Locate leukocytes (white blood cells).
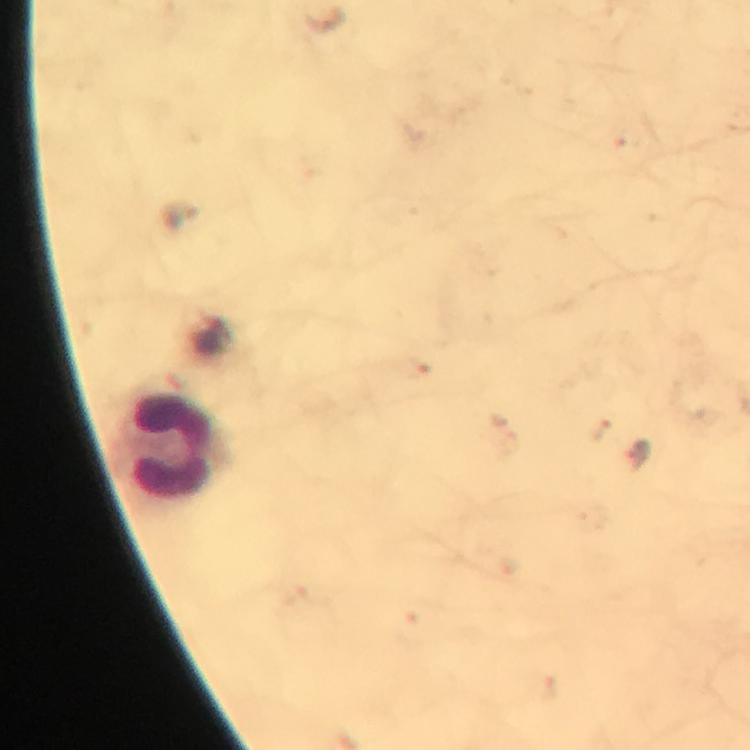

Approximate centers as [x, y] in pixels.
Leukocytes: [173, 445].

magnification = 100x
cropped from = one field of view
context = from a malaria diagnostic workup
image size = 750×750 pixels
immersion oil = applied
capture = smartphone mounted on the microscope
stain = Giemsa
preparation = thick blood film
Plasmodium parasites = none seen